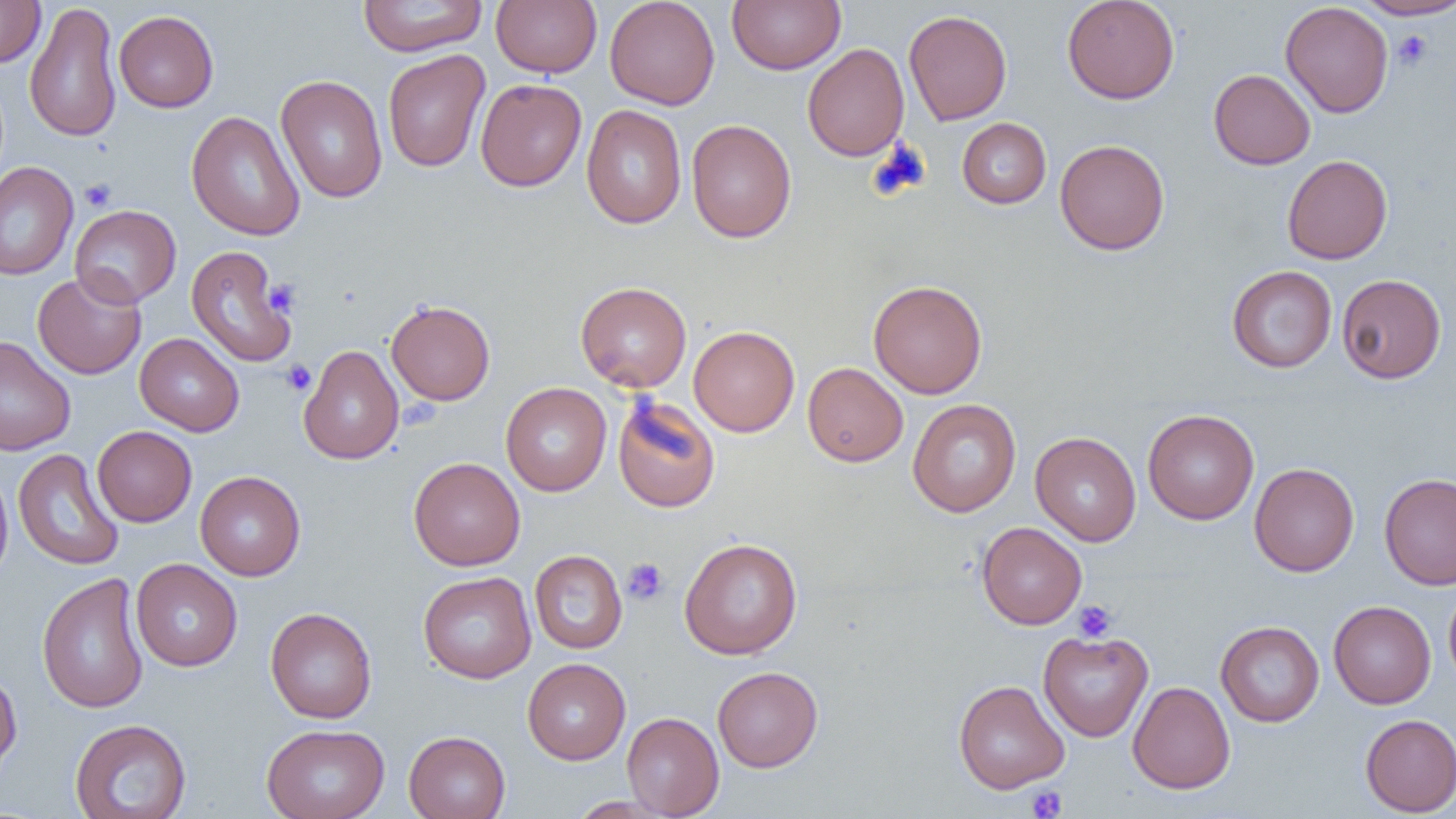
Approximate bounding boxes as named x1/y1/x2/y2 corners in pixels. Platelet locations (subset): (x1=1392, y1=30, x2=1433, y2=71), (x1=79, y1=178, x2=116, y2=211), (x1=264, y1=279, x2=300, y2=317), (x1=280, y1=359, x2=316, y2=396), (x1=622, y1=558, x2=669, y2=605), (x1=1073, y1=600, x2=1117, y2=642), (x1=1026, y1=785, x2=1068, y2=818). Uninfected red blood cell locations (subset): (x1=0, y1=0, x2=46, y2=68), (x1=356, y1=0, x2=488, y2=57), (x1=491, y1=0, x2=602, y2=78), (x1=604, y1=0, x2=720, y2=110), (x1=727, y1=0, x2=845, y2=75), (x1=1061, y1=0, x2=1180, y2=104), (x1=1355, y1=0, x2=1456, y2=21), (x1=1280, y1=1, x2=1393, y2=118), (x1=24, y1=2, x2=122, y2=143), (x1=903, y1=9, x2=1012, y2=125), (x1=113, y1=10, x2=218, y2=112), (x1=802, y1=43, x2=910, y2=162), (x1=382, y1=49, x2=490, y2=173), (x1=1208, y1=68, x2=1315, y2=169), (x1=275, y1=74, x2=388, y2=203), (x1=475, y1=79, x2=586, y2=191), (x1=581, y1=104, x2=686, y2=229), (x1=186, y1=110, x2=305, y2=241), (x1=957, y1=118, x2=1051, y2=208), (x1=686, y1=119, x2=796, y2=243), (x1=1055, y1=139, x2=1170, y2=255), (x1=1282, y1=154, x2=1393, y2=264), (x1=0, y1=162, x2=78, y2=280), (x1=70, y1=205, x2=181, y2=308), (x1=1227, y1=265, x2=1337, y2=373), (x1=32, y1=270, x2=147, y2=380), (x1=1336, y1=274, x2=1446, y2=383), (x1=868, y1=279, x2=987, y2=398), (x1=575, y1=281, x2=692, y2=392), (x1=386, y1=299, x2=495, y2=405), (x1=688, y1=325, x2=800, y2=436), (x1=135, y1=333, x2=244, y2=436), (x1=0, y1=336, x2=75, y2=456), (x1=298, y1=345, x2=404, y2=464), (x1=803, y1=362, x2=908, y2=467), (x1=500, y1=382, x2=612, y2=496), (x1=612, y1=394, x2=721, y2=513), (x1=907, y1=399, x2=1021, y2=517), (x1=1142, y1=409, x2=1259, y2=525), (x1=92, y1=425, x2=197, y2=527), (x1=1030, y1=431, x2=1141, y2=546), (x1=13, y1=449, x2=124, y2=571), (x1=409, y1=457, x2=525, y2=571), (x1=1249, y1=462, x2=1359, y2=576), (x1=0, y1=465, x2=13, y2=585), (x1=195, y1=470, x2=305, y2=581), (x1=1379, y1=473, x2=1456, y2=589), (x1=976, y1=522, x2=1087, y2=629), (x1=679, y1=537, x2=803, y2=660), (x1=529, y1=550, x2=627, y2=654), (x1=130, y1=558, x2=242, y2=672), (x1=418, y1=571, x2=536, y2=683), (x1=36, y1=572, x2=150, y2=714), (x1=1444, y1=583, x2=1456, y2=692), (x1=1328, y1=600, x2=1436, y2=709), (x1=265, y1=607, x2=377, y2=723), (x1=1215, y1=621, x2=1324, y2=727), (x1=1038, y1=630, x2=1153, y2=742), (x1=522, y1=658, x2=630, y2=764), (x1=712, y1=666, x2=823, y2=771), (x1=0, y1=669, x2=22, y2=779), (x1=953, y1=679, x2=1070, y2=794), (x1=1128, y1=680, x2=1235, y2=794), (x1=622, y1=712, x2=724, y2=818), (x1=1359, y1=714, x2=1456, y2=817), (x1=69, y1=718, x2=192, y2=818), (x1=261, y1=723, x2=389, y2=819), (x1=404, y1=730, x2=511, y2=819), (x1=568, y1=796, x2=675, y2=818). Slide-level diagnosis: no evidence of blood parasites. Captured at 1000x magnification. Single field of view. Image is 1456×819 pixels. Light microscopy. Thin blood smear.